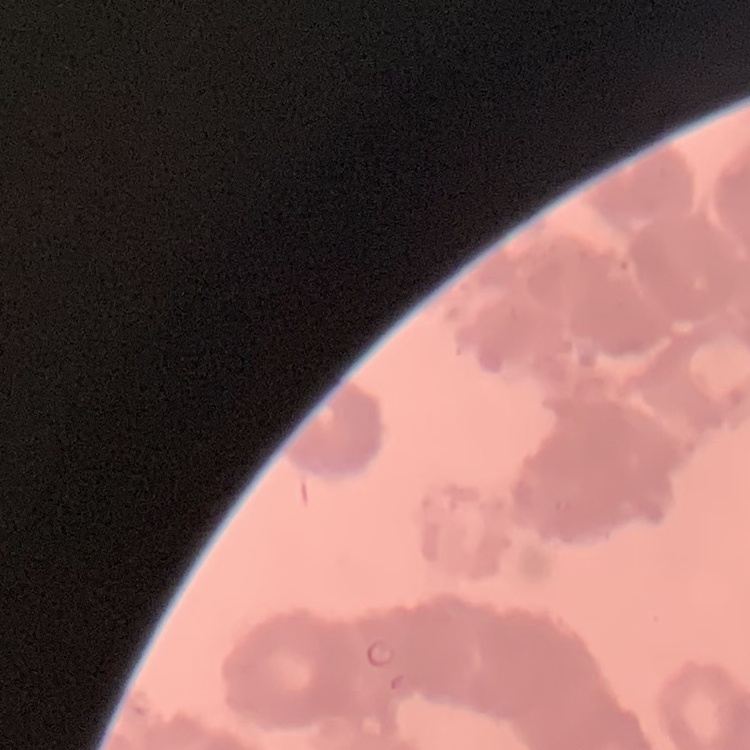
erythrocyte morphology = rouleaux formation
stain = Field's or Giemsa
preparation = thin peripheral smear
image type = one tile cut from a larger photomicrograph